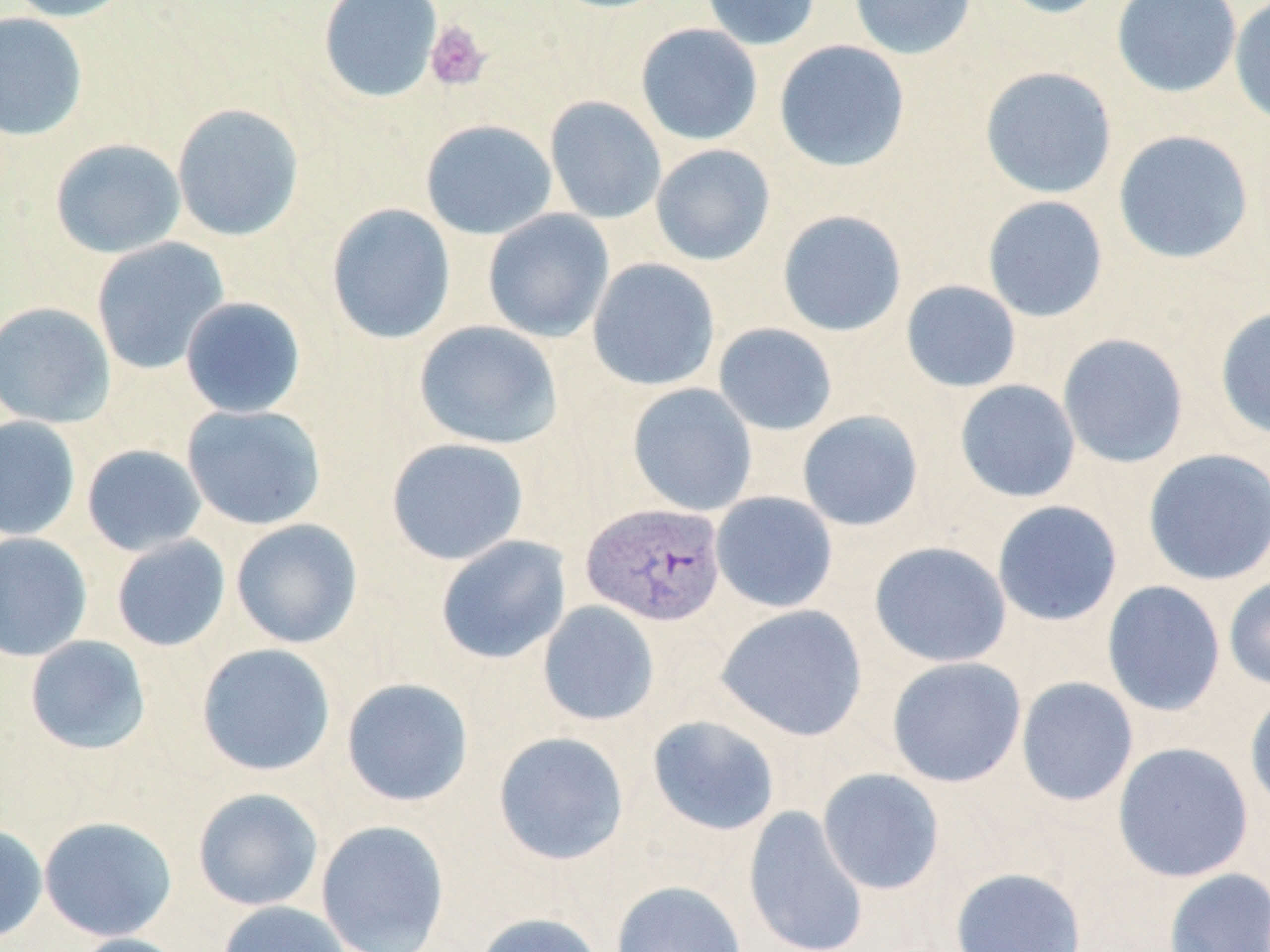

slide-level diagnosis = Plasmodium vivax
stain = May-Grünwald-Giemsa
platelet locations = approximate bounding boxes as (x1, y1, x2, y2) in pixels: (425, 20, 491, 91)
preparation = thin blood smear
Plasmodium vivax-infected red blood cell locations = approximate bounding boxes as (x1, y1, x2, y2) in pixels: (581, 502, 727, 626)
field of view = one of a larger specimen
image size = 1270×952 pixels
uninfected red blood cell locations = approximate bounding boxes as (x1, y1, x2, y2) in pixels: (4, 0, 137, 22), (318, 0, 443, 104), (701, 0, 821, 51), (849, 0, 977, 60), (991, 0, 1114, 19), (1112, 0, 1242, 99), (1229, 0, 1270, 128), (0, 12, 88, 141), (635, 23, 763, 146), (774, 39, 911, 172), (979, 66, 1117, 199), (545, 96, 666, 224), (171, 103, 305, 242), (420, 119, 557, 240), (1112, 129, 1255, 265), (49, 138, 186, 258), (650, 143, 776, 266), (981, 195, 1109, 323), (326, 202, 456, 345), (482, 209, 615, 343), (777, 209, 907, 337), (91, 238, 230, 375), (587, 258, 721, 391), (900, 280, 1022, 393), (179, 296, 307, 418), (0, 301, 116, 429), (1214, 304, 1270, 440), (413, 320, 562, 451), (713, 323, 838, 436), (1057, 333, 1189, 469), (954, 379, 1081, 503), (627, 383, 758, 516), (182, 404, 326, 530), (797, 410, 924, 531), (0, 416, 82, 541), (386, 437, 529, 565), (81, 444, 207, 557), (1142, 448, 1270, 586), (711, 491, 838, 613), (992, 500, 1123, 627), (230, 518, 364, 649), (0, 531, 93, 662), (111, 535, 231, 652), (435, 535, 571, 664), (869, 541, 1012, 668), (1224, 576, 1270, 692), (1102, 580, 1226, 717), (537, 601, 660, 726), (716, 604, 868, 742), (24, 635, 151, 755), (195, 642, 337, 776), (886, 656, 1026, 788), (1015, 676, 1139, 807), (341, 677, 475, 807), (1244, 688, 1270, 815), (646, 714, 781, 836), (492, 731, 630, 866), (1112, 741, 1254, 883), (816, 768, 945, 895), (192, 787, 324, 911), (743, 805, 869, 952), (39, 815, 177, 941), (315, 819, 451, 952), (0, 822, 49, 944), (949, 867, 1087, 952), (1163, 867, 1270, 952), (611, 880, 747, 952), (217, 900, 354, 952), (473, 911, 605, 952), (67, 933, 192, 952)
modality = light microscopy
magnification = 1000x